Name the parasite shown.
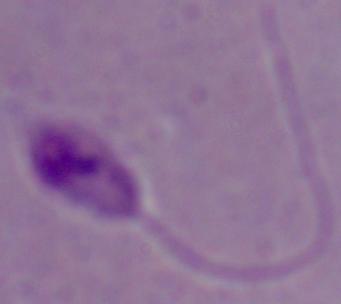

Leishmania.

Photomicrograph. Captured at 1000x magnification.